Locate every blood parasite and identify its species.
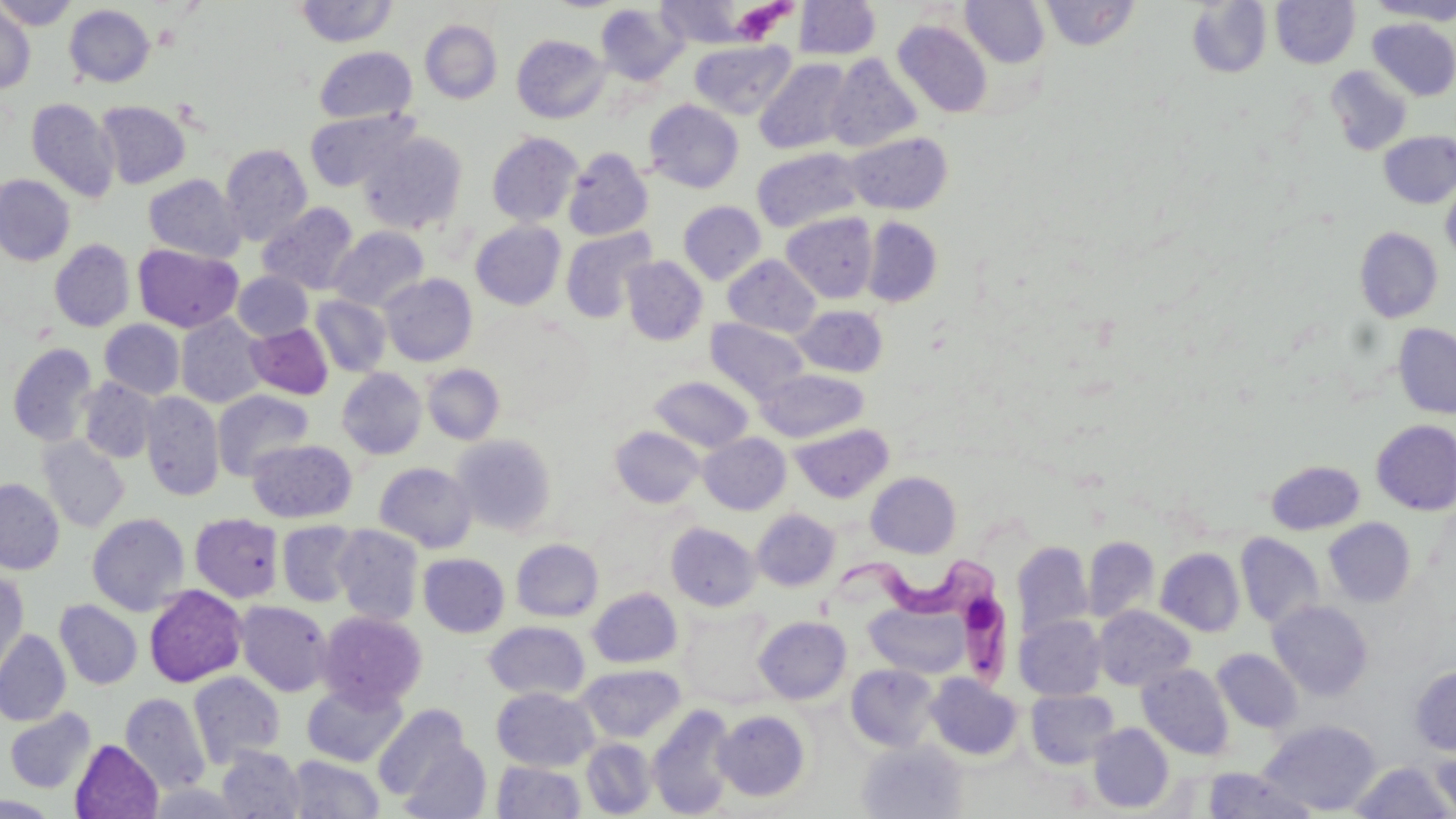

Approximate bounding boxes as [x1, y1, x2, y2] in pixels.
Trypanosoma brucei: [823, 542, 1018, 699].
No Plasmodium falciparum, Plasmodium ovale, Plasmodium malariae, Plasmodium vivax, or Babesia divergens observed.

Summary:
  - Uninfected red blood cell locations: [0, 0, 76, 30], [960, 0, 1050, 68], [1040, 0, 1140, 50], [1271, 0, 1360, 68], [1366, 0, 1456, 23], [293, 1, 399, 47], [655, 1, 755, 48], [794, 1, 881, 60], [1186, 1, 1272, 78], [595, 3, 688, 85], [64, 4, 155, 88], [0, 7, 35, 93], [1368, 18, 1456, 101], [419, 19, 502, 104], [893, 20, 992, 118], [512, 34, 609, 123], [689, 39, 796, 120], [314, 46, 417, 124], [825, 54, 923, 153], [754, 57, 855, 155], [1325, 66, 1413, 156], [26, 98, 120, 202], [644, 99, 744, 193], [96, 101, 191, 188], [304, 108, 417, 192], [358, 131, 468, 234], [1379, 131, 1456, 208], [486, 132, 582, 227], [846, 132, 952, 214], [220, 143, 313, 245], [563, 147, 654, 241], [751, 147, 864, 233], [0, 174, 75, 266], [143, 174, 246, 263], [1441, 176, 1456, 264], [678, 201, 767, 284], [257, 202, 360, 295], [781, 212, 877, 303], [862, 217, 942, 306], [470, 221, 566, 310], [329, 227, 429, 311], [1354, 227, 1443, 323], [560, 228, 656, 323], [49, 239, 135, 332], [132, 244, 243, 333], [722, 255, 821, 337], [621, 256, 708, 345], [233, 272, 313, 341], [379, 273, 477, 366], [311, 295, 391, 377], [792, 305, 888, 377], [175, 314, 269, 408], [706, 317, 809, 405], [99, 319, 184, 399], [245, 323, 333, 399], [1394, 323, 1456, 418], [7, 342, 98, 447], [422, 364, 505, 445], [336, 368, 427, 460], [757, 369, 868, 442], [649, 376, 753, 453], [78, 378, 158, 463], [212, 389, 314, 481], [140, 392, 224, 501], [1371, 419, 1456, 515], [791, 424, 893, 503], [610, 426, 705, 508], [698, 433, 790, 514], [451, 434, 557, 536], [37, 435, 130, 532], [247, 439, 357, 523], [1266, 460, 1365, 535], [375, 462, 477, 553], [866, 472, 961, 557], [0, 479, 64, 574], [752, 508, 840, 591], [189, 512, 284, 603], [87, 513, 190, 616], [1323, 518, 1417, 607], [277, 520, 361, 607], [666, 522, 761, 611], [333, 525, 424, 625], [1235, 533, 1324, 629], [1083, 536, 1159, 624], [511, 539, 603, 621], [1012, 542, 1093, 644], [1155, 548, 1245, 637], [419, 553, 509, 637], [0, 571, 29, 681], [144, 585, 247, 688], [588, 587, 682, 668], [55, 599, 142, 690], [235, 600, 333, 696], [1267, 600, 1373, 701], [867, 602, 968, 678], [678, 605, 781, 708], [1093, 605, 1195, 691], [317, 610, 426, 709], [1016, 615, 1106, 701], [754, 616, 851, 704], [484, 621, 590, 701], [0, 629, 71, 727], [1212, 649, 1303, 733], [577, 664, 686, 743], [846, 664, 941, 751], [1138, 664, 1233, 759], [1409, 665, 1456, 755], [188, 672, 285, 768], [926, 673, 1022, 760], [301, 680, 407, 768], [492, 686, 598, 771], [1026, 689, 1120, 769], [120, 692, 210, 796], [372, 704, 475, 805], [647, 705, 737, 818], [4, 707, 96, 794], [713, 710, 810, 801], [1260, 719, 1383, 815], [1088, 723, 1174, 813], [582, 738, 656, 817], [396, 739, 492, 819], [857, 739, 968, 819], [70, 740, 163, 819], [1430, 744, 1456, 819], [216, 745, 306, 818], [287, 754, 384, 818], [492, 760, 585, 818], [1349, 762, 1454, 818], [1200, 767, 1314, 818], [148, 783, 247, 818], [0, 795, 59, 818]
  - Platelet locations: [728, 1, 791, 44]
  - Slide-level diagnosis: Trypanosoma brucei
  - Modality: light microscopy
  - Stain: May-Grünwald-Giemsa
  - Image size: 1456×819 pixels
  - Field of view: one of a larger specimen
  - Preparation: thin blood smear
  - Magnification: 1000x